State the blood parasite species.
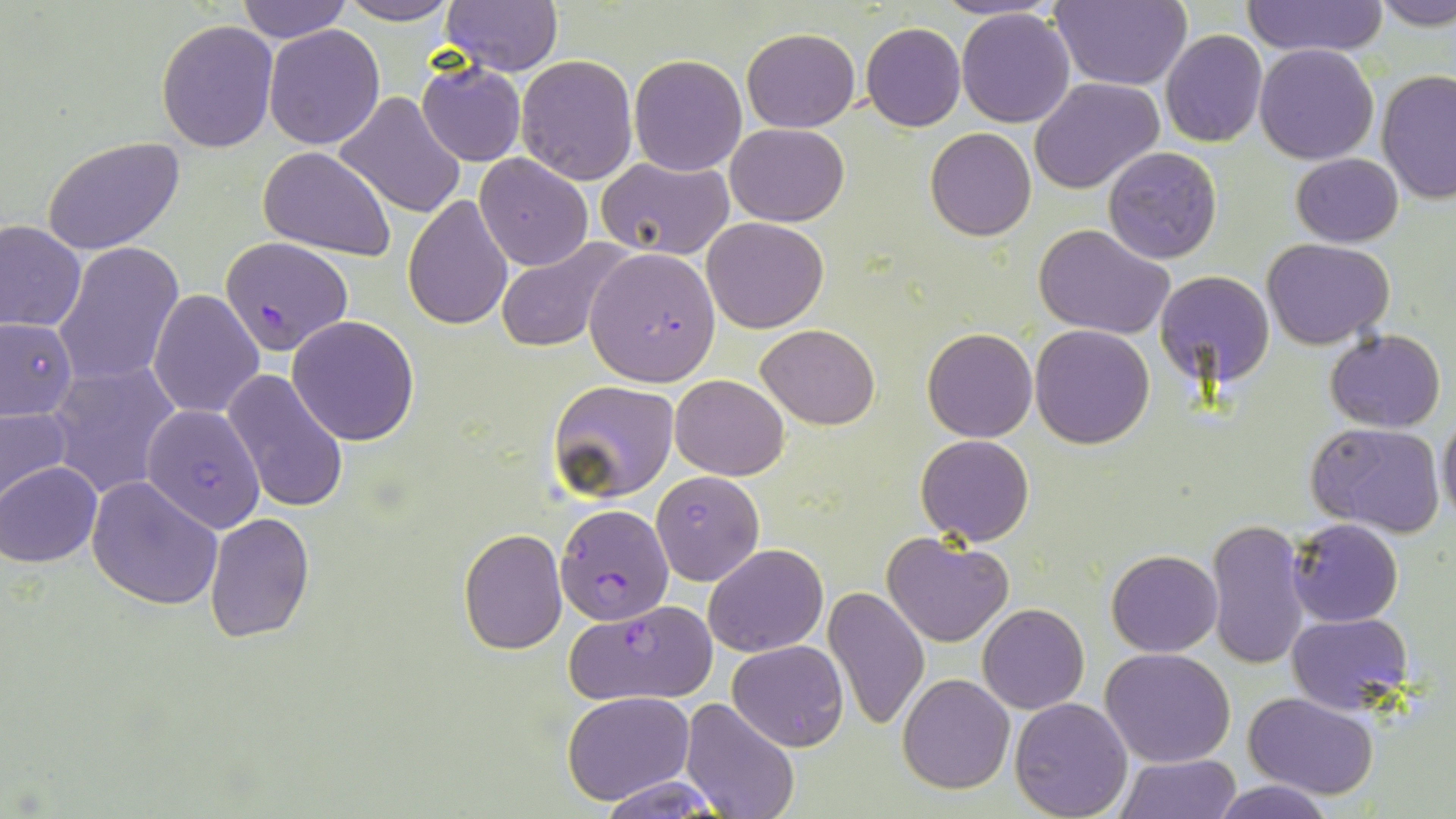
Plasmodium falciparum.

stain = May-Grünwald-Giemsa
Plasmodium falciparum-infected red blood cell locations = approximate bounding boxes as (x1,y1)-(x2,y2) corner pairs in pixels: (219,234)-(354,354), (583,248)-(720,386), (554,506)-(673,624), (564,600)-(720,708)
preparation = thin blood smear
field of view = single
uninfected red blood cell locations = approximate bounding boxes as (x1,y1)-(x2,y2) corner pairs in pixels: (236,0)-(352,43), (442,0)-(563,77), (1049,0)-(1190,91), (1373,0)-(1456,30), (333,1)-(460,25), (1240,1)-(1388,56), (956,7)-(1076,127), (155,20)-(277,153), (861,23)-(966,131), (263,24)-(385,149), (742,28)-(860,132), (1161,29)-(1267,147), (1254,44)-(1378,165), (627,53)-(748,176), (516,54)-(638,185), (416,62)-(526,166), (1376,70)-(1456,207), (1032,77)-(1165,196), (334,91)-(467,218), (725,123)-(849,227), (925,129)-(1036,241), (42,134)-(186,254), (1102,146)-(1223,266), (258,147)-(398,261), (474,153)-(594,271), (1291,153)-(1404,247), (597,157)-(734,258), (422,170)-(583,314), (403,193)-(514,331), (702,217)-(830,333), (0,219)-(86,333), (1034,223)-(1172,339), (494,238)-(632,353), (1265,238)-(1393,348), (54,241)-(184,389), (1155,269)-(1274,386), (149,290)-(265,417), (0,316)-(78,423), (287,316)-(420,445), (757,322)-(878,430), (1029,324)-(1155,448), (922,328)-(1036,442), (1324,329)-(1448,433), (48,360)-(181,499), (222,368)-(349,515), (670,374)-(789,479), (546,380)-(679,505), (0,402)-(73,509), (139,404)-(269,541), (1437,410)-(1456,525), (1305,419)-(1447,537), (916,434)-(1035,547), (1,462)-(101,567), (652,470)-(763,586), (86,476)-(222,610), (204,511)-(315,643), (1206,517)-(1311,670), (1287,517)-(1404,627), (458,529)-(568,655), (882,532)-(1014,648), (703,543)-(829,658), (1106,550)-(1222,657), (824,584)-(930,731), (977,603)-(1089,714), (1286,612)-(1412,715), (727,640)-(848,752), (1101,647)-(1236,767), (897,673)-(1015,793), (562,691)-(694,805), (1244,692)-(1380,801), (1008,696)-(1133,817), (680,697)-(799,819), (1116,754)-(1239,819), (597,773)-(728,817), (1210,778)-(1333,819)
modality = light microscopy
image size = 1456×819 pixels
magnification = 1000x